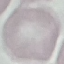
Summary:
  - Malaria status: uninfected
  - Stain: Giemsa
  - Preparation: thin smear
  - Image type: cell patch, automatically extracted from a larger field of view and resized to 64 × 64 pixels
  - Capture: smartphone camera at the microscope eyepiece